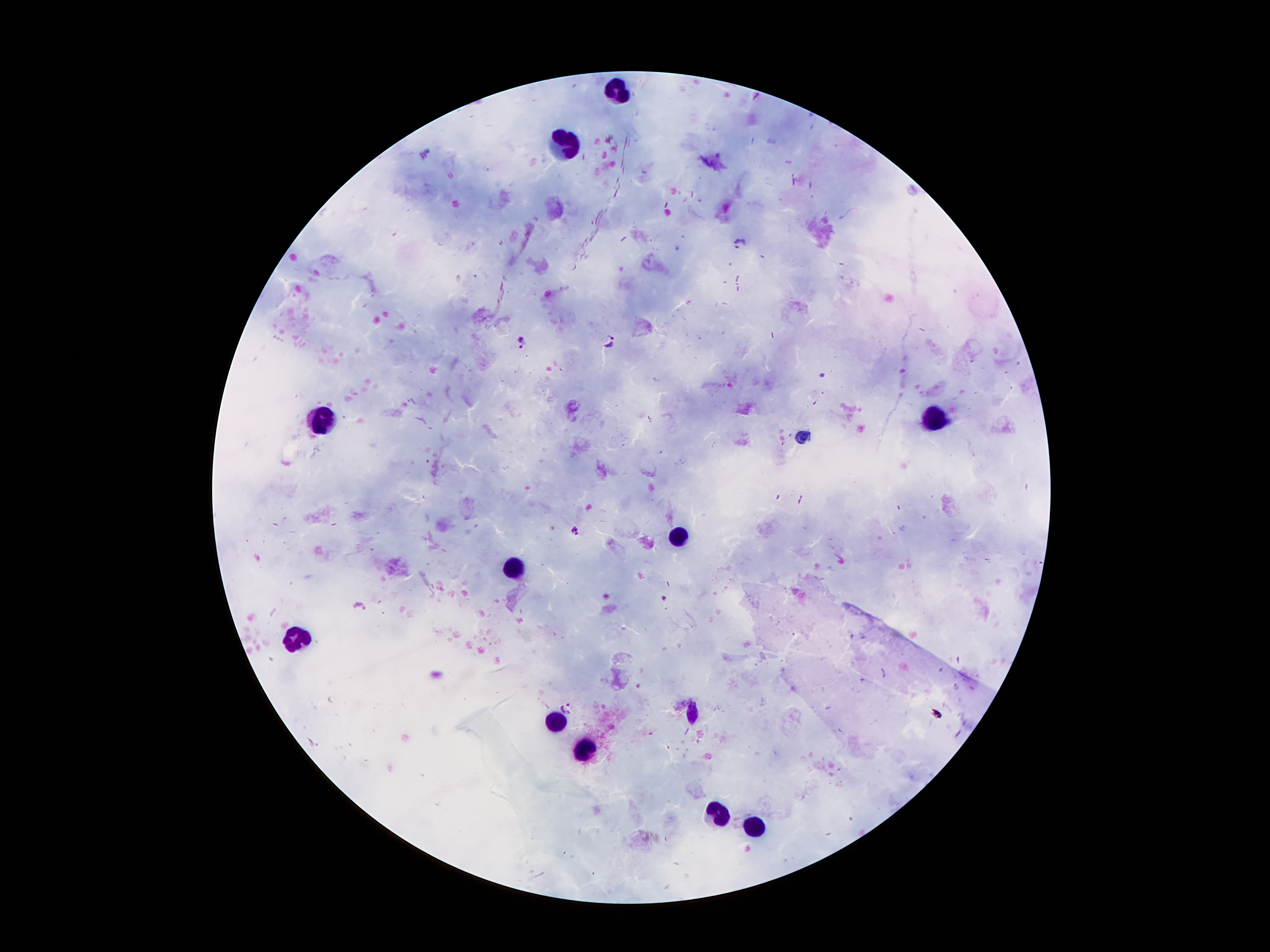 Approximate centers as (x, y) in pixels. Leukocyte locations: (620, 90), (565, 145), (937, 416), (323, 420), (678, 535), (510, 569), (296, 636), (689, 716), (554, 722), (586, 751), (716, 814), (756, 827). Malaria parasite locations: (738, 243), (522, 340), (611, 341), (574, 530), (360, 606), (568, 706). Thick blood smear. Single field of view. Image is 1270×952 pixels. 100x magnification. Photographed through the microscope eyepiece with a smartphone camera. Patient malaria status: positive for Plasmodium falciparum. Giemsa stain.